State which parasite is depicted.
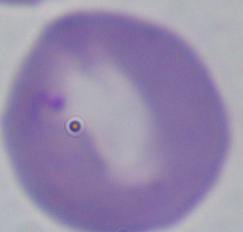
This is Babesia.

Summary:
  - Magnification: 1000x
  - Modality: photomicrograph